State the preparation type.
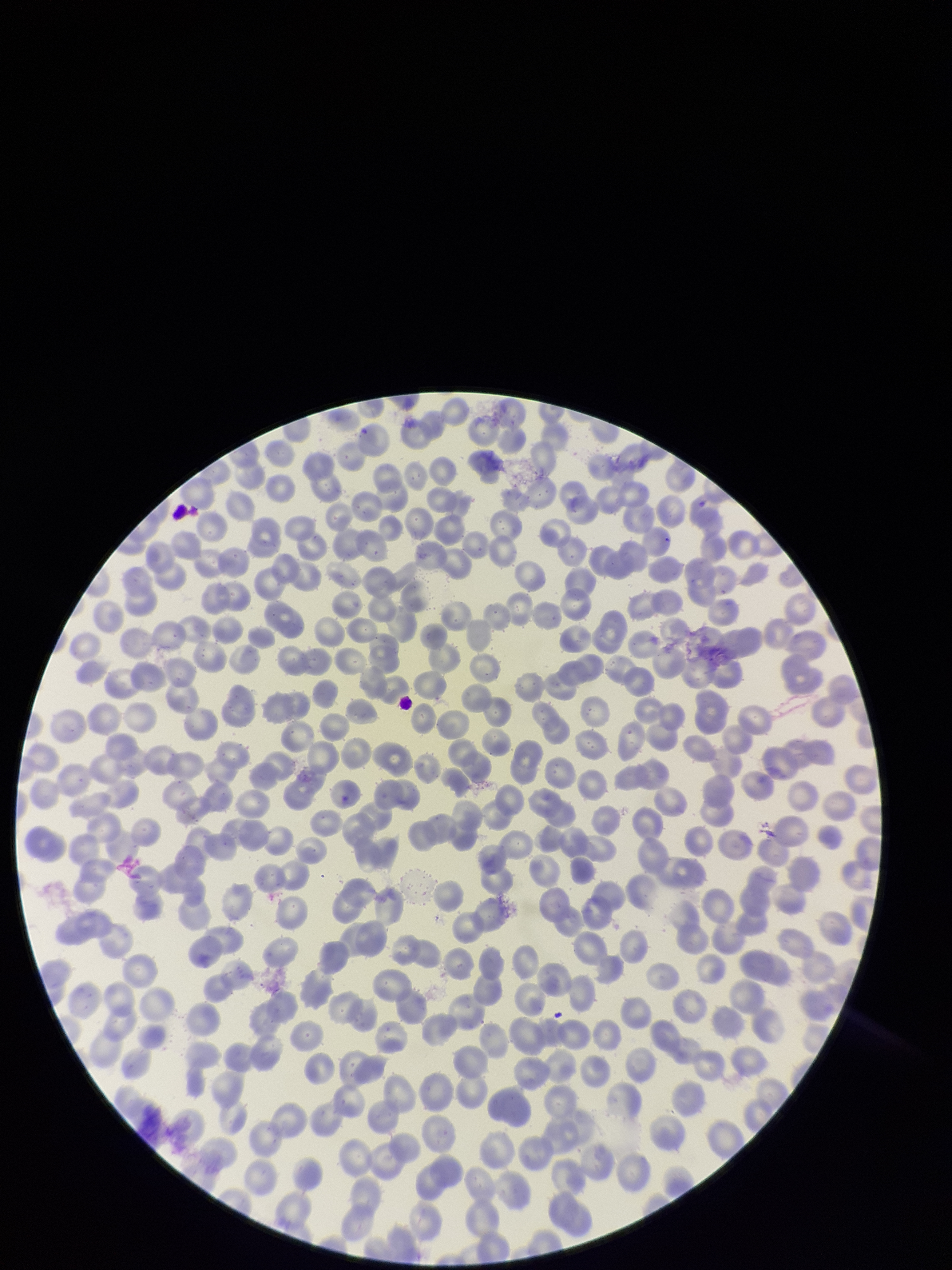
Thin.

Summary:
  - Parasitized red blood cell count: 0
  - Image size: 952×1270 pixels
  - Species reported for this patient: Plasmodium falciparum
  - Red blood cell count: 343
  - Field of view: single
  - Parasitized red blood cells: none detected
  - Capture: smartphone photograph through the microscope eyepiece
  - Patient malaria status: positive
  - Stain: Giemsa